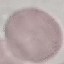 Result: no malaria parasites detected. Giemsa stain. Thin blood smear. Photographed with a smartphone camera at the microscope eyepiece. Automatically extracted cell patch, resized to 64 × 64 pixels.